Identify the parasite.
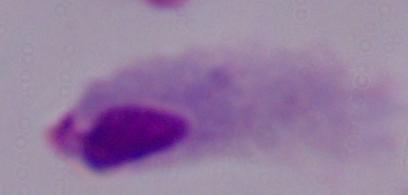
This is a trichomonad.

Summary:
  - Magnification: 1000x
  - Modality: micrograph